Locate every blood parasite and identify its species.
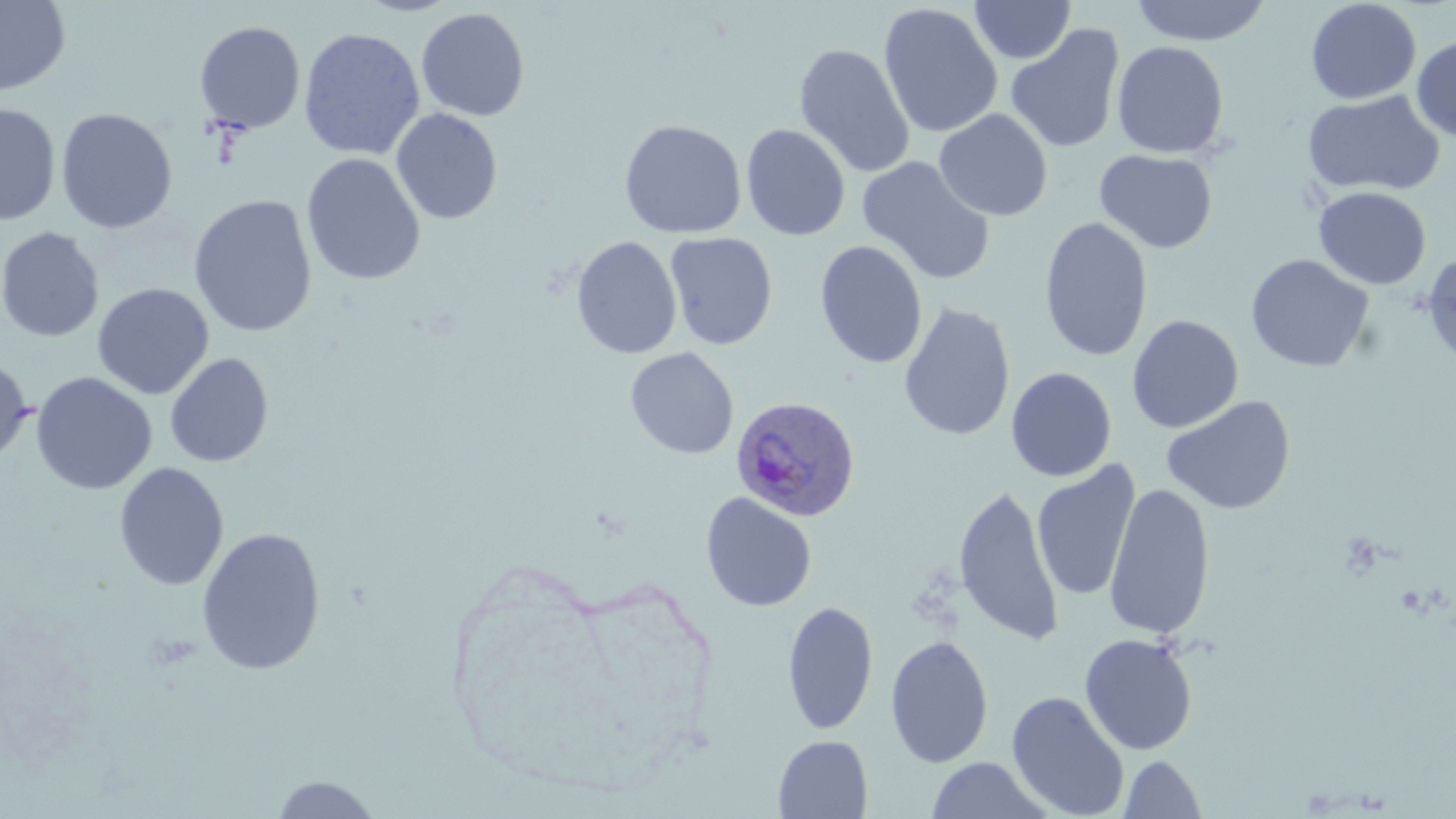
Approximate bounding boxes as (x1, y1, x2, y2) in pixels.
Plasmodium ovale-infected red blood cells: (730, 394, 861, 522).
No Plasmodium falciparum, Plasmodium malariae, Plasmodium vivax, Babesia divergens, or Trypanosoma brucei observed.

slide-level diagnosis = Plasmodium ovale
field of view = single
image size = 1456×819 pixels
modality = light microscopy
magnification = 1000x
stain = May-Grünwald-Giemsa
preparation = thin blood film
uninfected red blood cell locations = approximate bounding boxes as (x1, y1, x2, y2) in pixels: (969, 0, 1076, 64), (1129, 0, 1273, 46), (1305, 0, 1421, 105), (0, 1, 71, 97), (878, 3, 1003, 138), (416, 8, 530, 121), (194, 20, 306, 134), (1005, 23, 1125, 154), (299, 27, 425, 160), (1411, 35, 1456, 142), (1111, 41, 1229, 159), (794, 43, 915, 179), (1302, 89, 1446, 197), (0, 102, 61, 226), (55, 108, 178, 234), (391, 108, 503, 225), (934, 109, 1053, 221), (619, 119, 747, 239), (740, 124, 851, 241), (1094, 149, 1217, 253), (301, 154, 426, 286), (857, 156, 996, 285), (1313, 186, 1431, 290), (188, 195, 317, 337), (1039, 216, 1153, 362), (0, 227, 104, 342), (664, 232, 778, 350), (571, 236, 682, 360), (814, 240, 928, 369), (1421, 250, 1456, 367), (1245, 254, 1375, 373), (92, 283, 214, 400), (898, 302, 1016, 441), (1126, 315, 1244, 433), (625, 347, 739, 460), (165, 352, 274, 468), (0, 356, 34, 467), (1005, 367, 1117, 482), (30, 372, 157, 495), (1161, 395, 1295, 516), (1032, 461, 1141, 602), (113, 462, 229, 590), (952, 483, 1063, 647), (1104, 483, 1216, 640), (700, 492, 817, 612), (196, 527, 326, 676), (782, 600, 879, 735), (1079, 633, 1198, 755), (885, 635, 994, 768), (1007, 691, 1129, 819), (772, 735, 873, 818), (1118, 754, 1208, 818), (925, 757, 1052, 818), (267, 774, 386, 818)